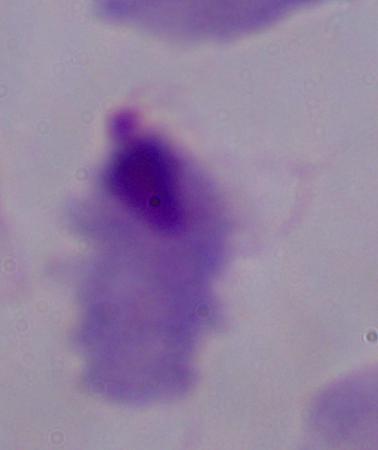
modality = photomicrograph
identification = trichomonad
magnification = 1000x